Assess this cell for malaria.
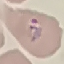

It is parasitized.

capture = smartphone through the microscope eyepiece
preparation = thin blood smear
stain = Giemsa
image type = automatically extracted cell patch, resized to 64 × 64 pixels